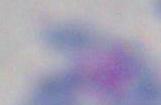
Summary:
  - Modality: micrograph
  - Magnification: 1000x
  - Identification: Toxoplasma gondii